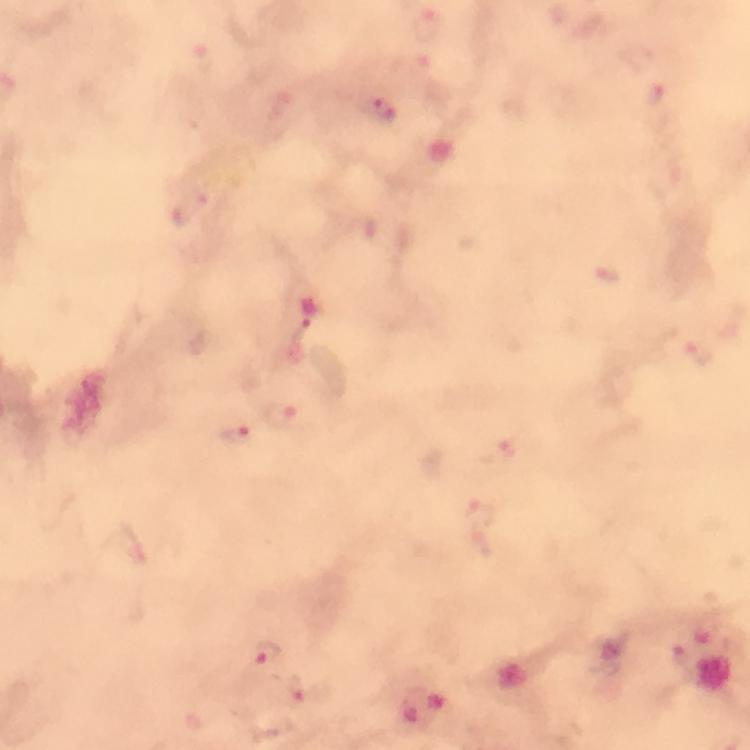
capture = smartphone photograph through a microscope
magnification = 100x
Plasmodium parasite locations = approximate centers as [x, y] in pixels: [427, 24], [381, 108], [190, 208], [701, 351], [280, 414], [232, 431], [508, 449], [482, 515], [267, 653], [300, 689]
context = from a malaria diagnostic workup
preparation = thick blood smear
stain = Giemsa
immersion oil = used
image size = 750×750 pixels
cropped from = a single field of view